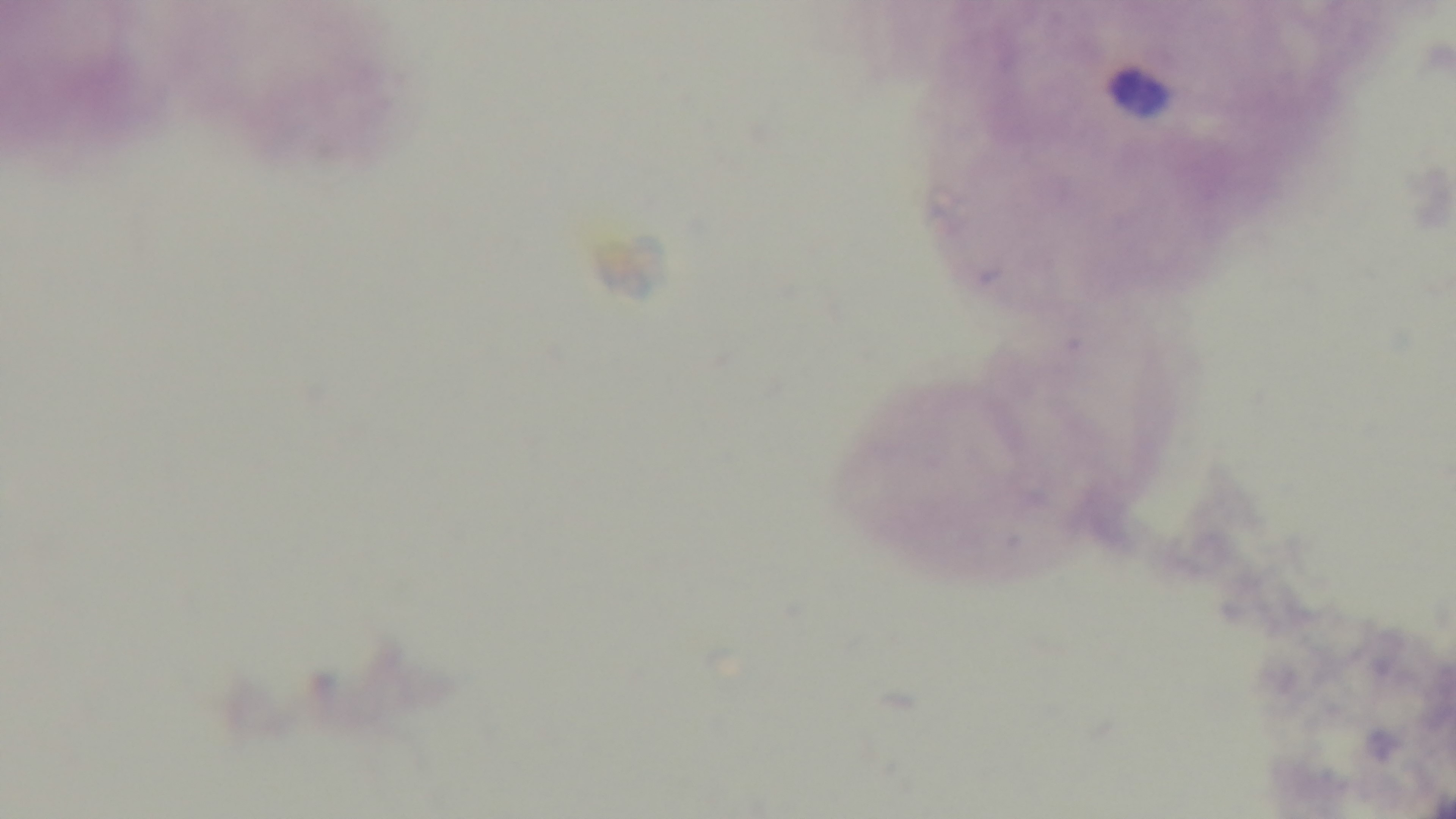

Single field of view. Mounted 4K digital camera. Oil-immersion objective, 100x. Giemsa stain. Malaria status: negative. Photomicrograph. Preparation: thick blood film.